Assess this cell for malaria.
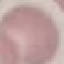

Uninfected.

Summary:
  - Stain: Giemsa
  - Image type: automatically extracted cell patch, resized to 64 × 64 pixels
  - Capture: smartphone camera at the microscope eyepiece
  - Preparation: thin blood film